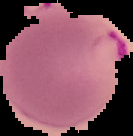

Cell region segmented out of the field of view; the surrounding area is masked to black. From a thin blood film. Image is 133×136 pixels. Result: malaria parasites detected.